Report the malaria status.
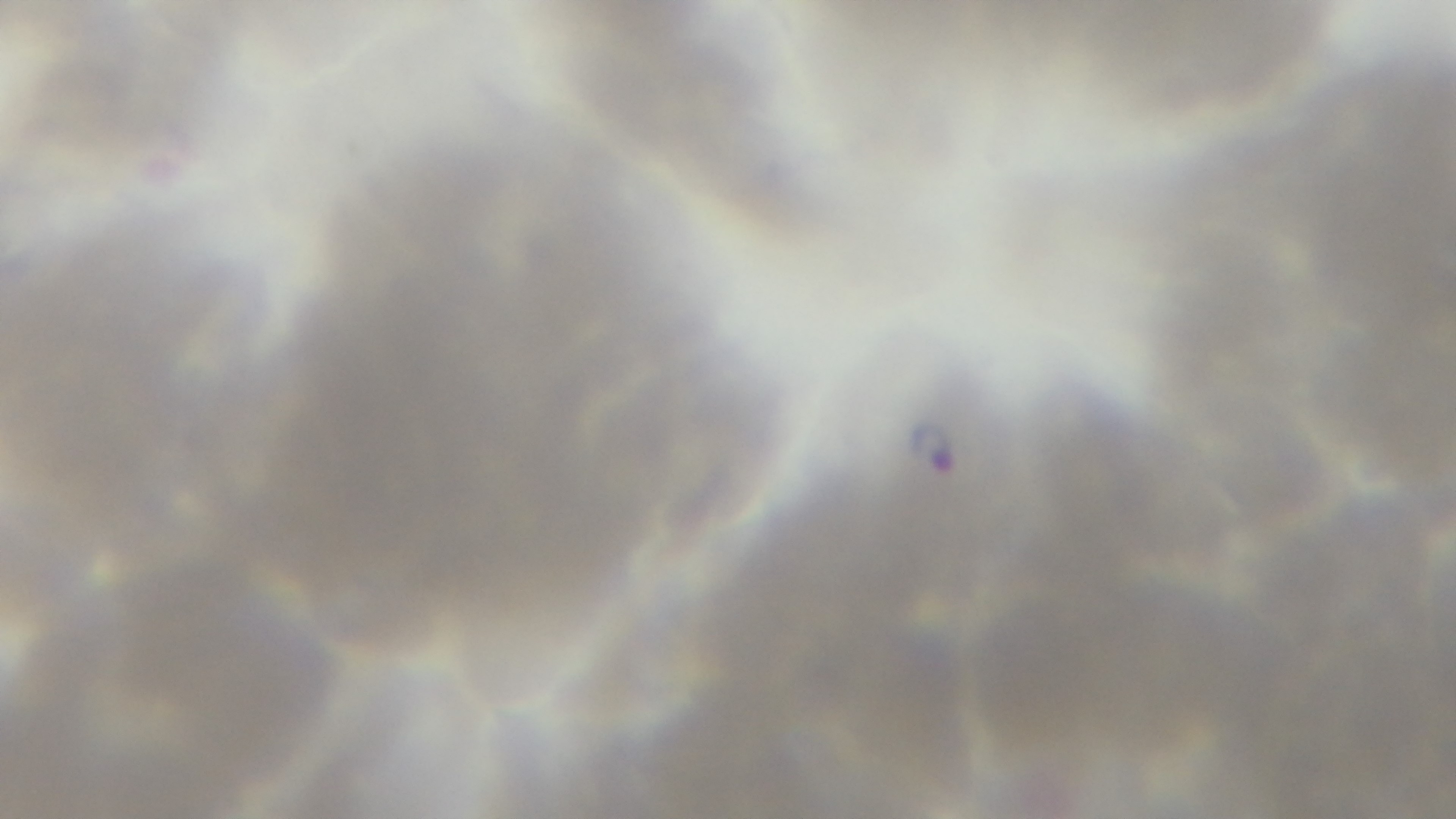
Positive.

field of view = one from the slide
preparation = thin blood film
modality = light microscopy
stain = Giemsa
objective = 100x oil immersion
capture = mounted 4K digital camera